Classify this cell by malaria status.
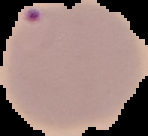

It is parasitized.

Segmented cell region on a black background. Image is 148×136 pixels. From a thin blood smear.